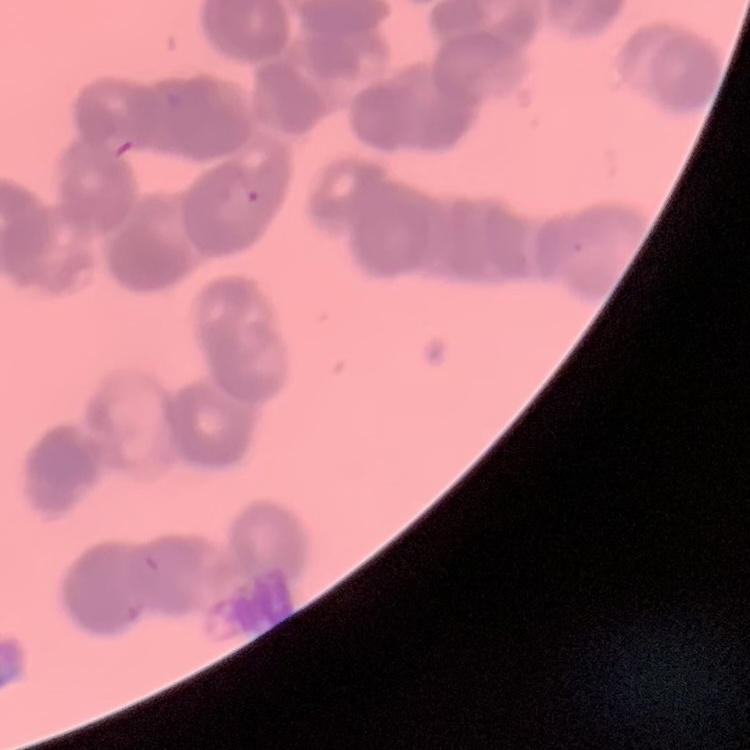
Summary:
  - Erythrocyte morphology: rouleaux formation
  - Image type: one tile cut from a larger photomicrograph
  - Stain: Field's or Giemsa
  - Preparation: thin peripheral smear